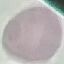
Malaria status: uninfected. Acquired by smartphone through the microscope eyepiece. Giemsa-stained preparation. Thin blood smear. Automatically extracted cell patch, resized to 64 × 64 pixels.